Classify this cell by malaria status.
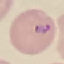

It is parasitized.

Photographed with a smartphone camera at the microscope eyepiece. Thin blood smear. Giemsa stain. Automatically extracted cell patch, resized to 64 × 64 pixels.